Name the parasite shown.
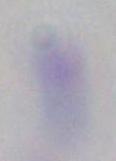
Toxoplasma gondii.

Summary:
  - Modality: photomicrograph
  - Magnification: 1000x